Report the malaria status of this cell.
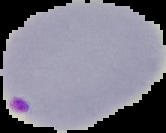
Parasitized.

Segmented cell region on a black background. Image is 166×133 pixels. From a thin blood smear.